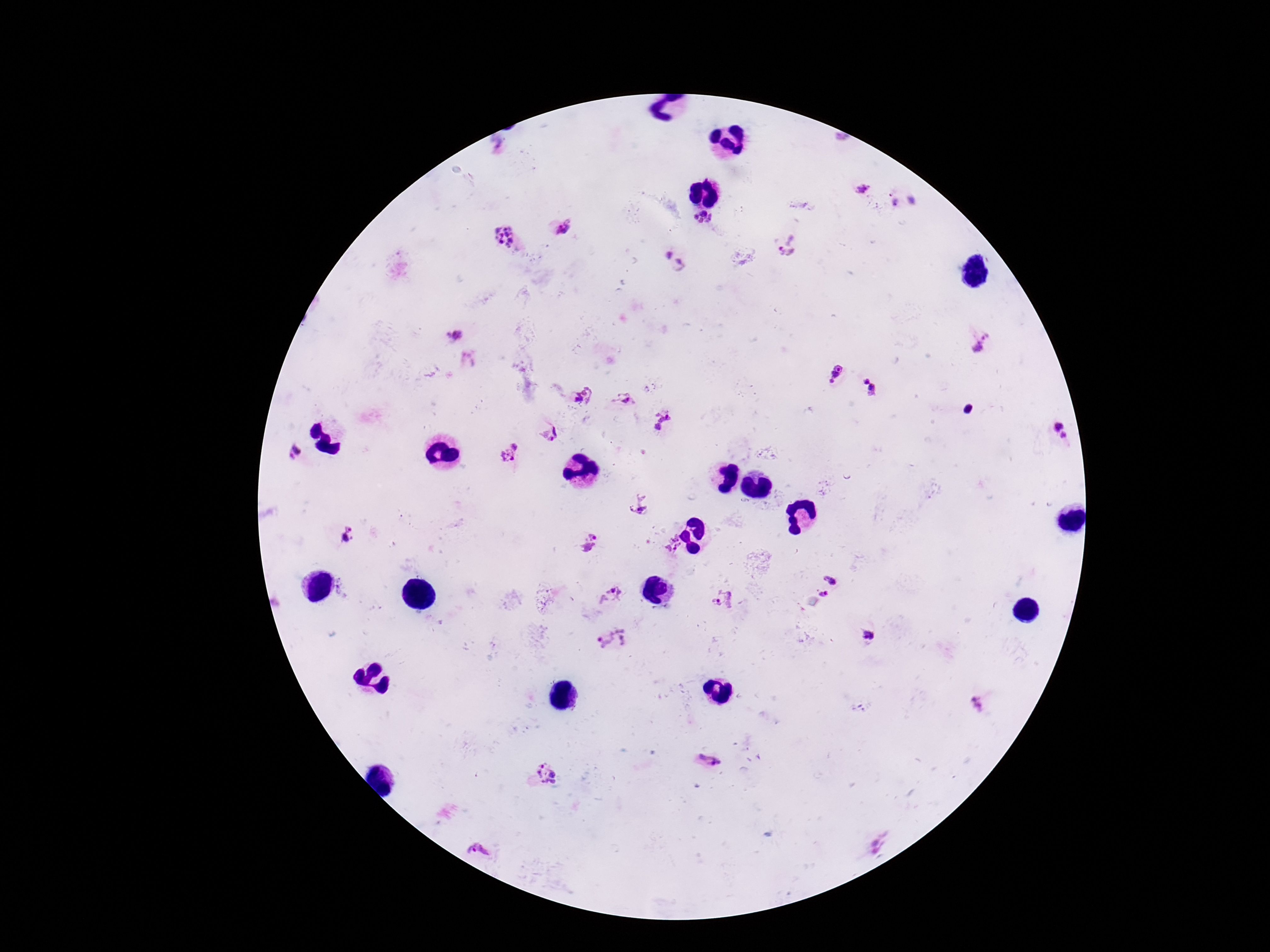 Approximate object centers, in pixels from the top-left corner. Plasmodium parasite locations: (x=862, y=188), (x=703, y=217), (x=566, y=227), (x=506, y=236), (x=791, y=245), (x=669, y=255), (x=678, y=260), (x=455, y=336), (x=979, y=343), (x=467, y=359), (x=835, y=372), (x=870, y=388), (x=584, y=395), (x=625, y=400), (x=664, y=422), (x=1059, y=432), (x=549, y=434), (x=516, y=444), (x=295, y=453), (x=507, y=456), (x=640, y=504), (x=349, y=528), (x=352, y=537), (x=345, y=538), (x=591, y=543), (x=672, y=543), (x=832, y=579), (x=824, y=594), (x=609, y=597), (x=722, y=599), (x=869, y=635), (x=613, y=638), (x=979, y=702), (x=708, y=759), (x=547, y=774), (x=877, y=842), (x=479, y=849). 100x magnification. One field from this slide. Giemsa-stained preparation. Patient malaria status: positive. Smartphone photograph taken through the microscope eyepiece. Thick peripheral-blood smear. Image is 1270×952 pixels.